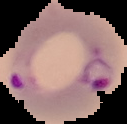

Summary:
  - Preparation: thin blood film
  - Image size: 127×124 pixels
  - Result: malaria parasites identified
  - Image type: segmented cell region on a black background